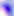

Summary:
  - Modality: photomicrograph
  - Magnification: 400x
  - Identification: Toxoplasma gondii